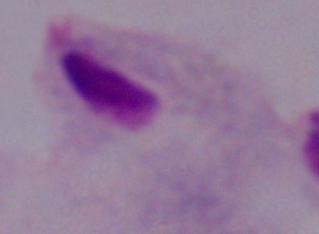
Summary:
  - Magnification: 1000x
  - Modality: micrograph
  - Identification: trichomonad